Assess this cell for malaria.
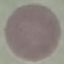

Uninfected.

stain = Giemsa
image type = cell patch, automatically extracted from a larger field of view and resized to 64 × 64 pixels
preparation = thin smear
capture = smartphone camera at the microscope eyepiece